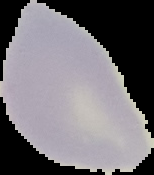
{
  "image_type": "segmented cell region on a black background",
  "malaria_status": "uninfected",
  "preparation": "thin blood film",
  "image_size": "154×175 pixels"
}